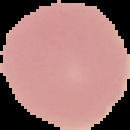

The area outside the segmented cell region is set to black. From a thin blood film. Image is 130×130 pixels. Result: no malaria parasites detected.